Assess this cell for malaria.
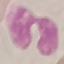

Uninfected.

{
  "image_type": "cell patch, automatically extracted from a larger field of view and resized to 64 × 64 pixels",
  "stain": "Giemsa",
  "capture": "smartphone camera at the microscope eyepiece",
  "preparation": "thin blood film"
}